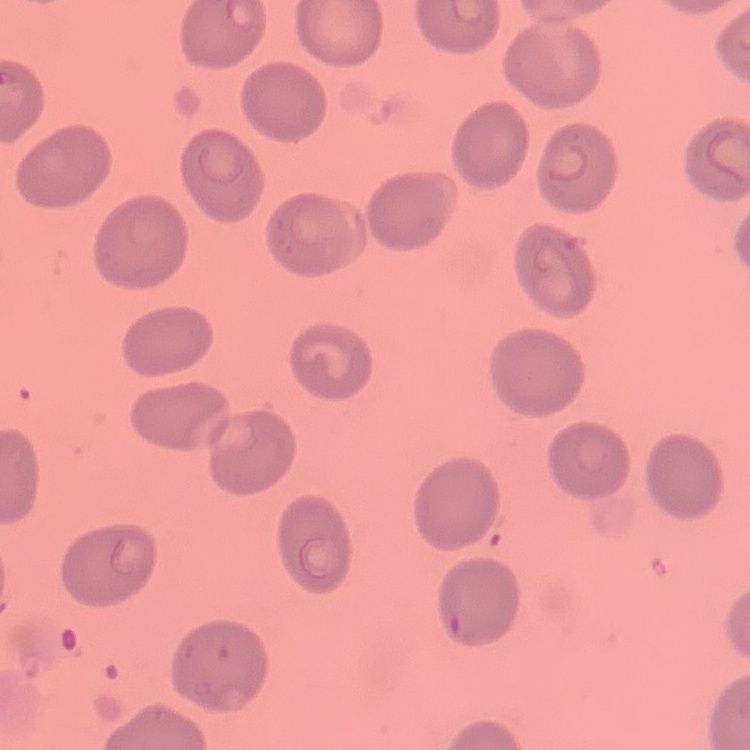
The erythrocytes exhibit no rouleaux formation. Square crop of a larger photomicrograph. Field's or Giemsa stain. Thin peripheral smear.